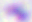
Summary:
  - Modality: micrograph
  - Identification: Toxoplasma gondii
  - Magnification: 400x